Evaluate for Plasmodium parasites.
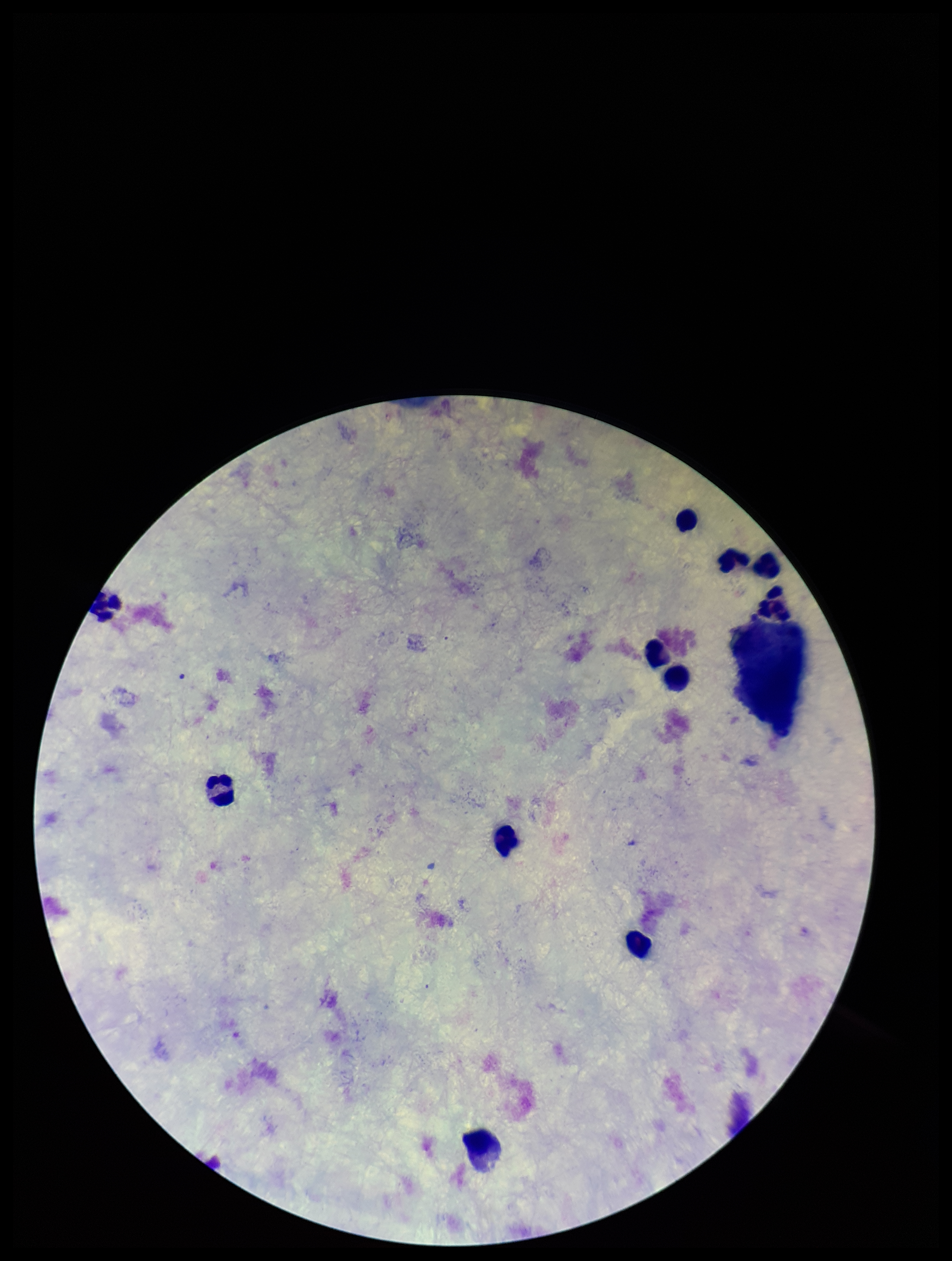
None detected.

preparation: thick smear
field_of_view: single
image_size: 952×1261 pixels
leukocyte_count: 11
capture: smartphone photograph through the microscope eyepiece
patient_malaria_status: negative
parasite_count: 0
stain: Giemsa